Assess this cell for malaria.
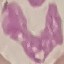
Uninfected.

Summary:
  - Capture: smartphone through the microscope eyepiece
  - Stain: Giemsa
  - Preparation: thin blood film
  - Image type: automatically extracted cell patch, resized to 64 × 64 pixels